Point out each Plasmodium parasite and each leukocyte.
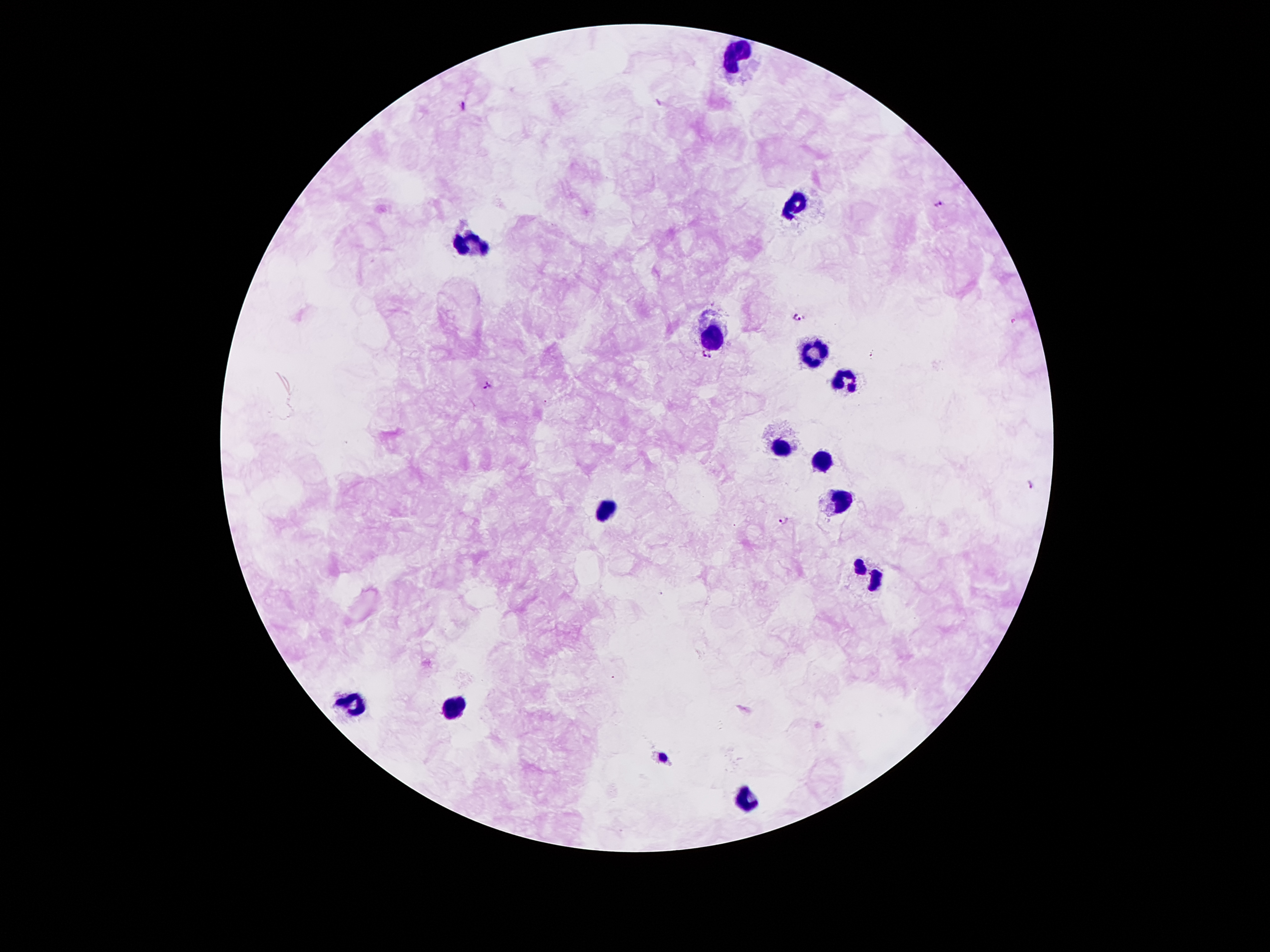

Approximate centers as (x, y) in pixels.
Plasmodium parasites: (465, 105), (939, 203), (796, 318), (705, 356), (489, 384), (1030, 486), (786, 519).
Leukocytes: (738, 50), (794, 206), (474, 240), (715, 330), (819, 352), (841, 381), (782, 447), (822, 462), (841, 503), (606, 509), (875, 574), (348, 705), (455, 705), (746, 800).

{
  "stain": "Giemsa",
  "image_size": "1270×952 pixels",
  "magnification": "100x",
  "field_of_view": "one from this slide",
  "preparation": "thick peripheral-blood smear",
  "patient_malaria_status": "infected with Plasmodium falciparum",
  "capture": "smartphone camera through the microscope eyepiece"
}